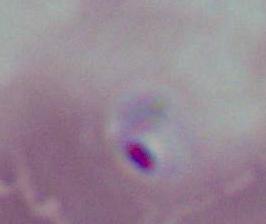

Micrograph. Captured at either 400x or 1000x magnification. A Plasmodium parasite is shown.